Comment on the morphology of the red blood cells.
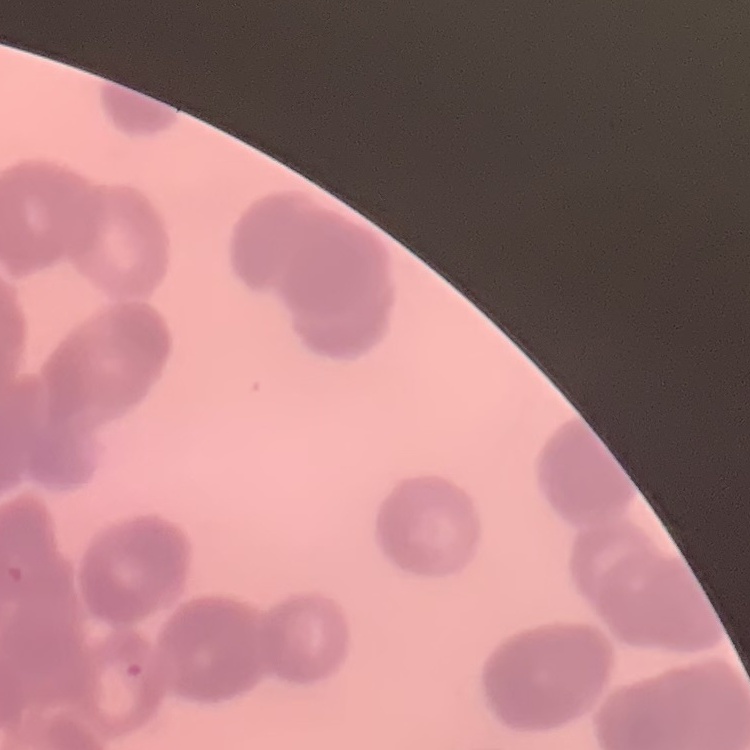
They show rouleaux formation.

Summary:
  - Image type: square crop of a larger photomicrograph
  - Preparation: thin peripheral smear
  - Stain: Field's or Giemsa